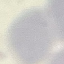

result = no malaria parasites seen
capture = smartphone through the microscope eyepiece
image type = cell patch, automatically extracted from a larger field of view and resized to 64 × 64 pixels
preparation = thin smear
stain = Giemsa